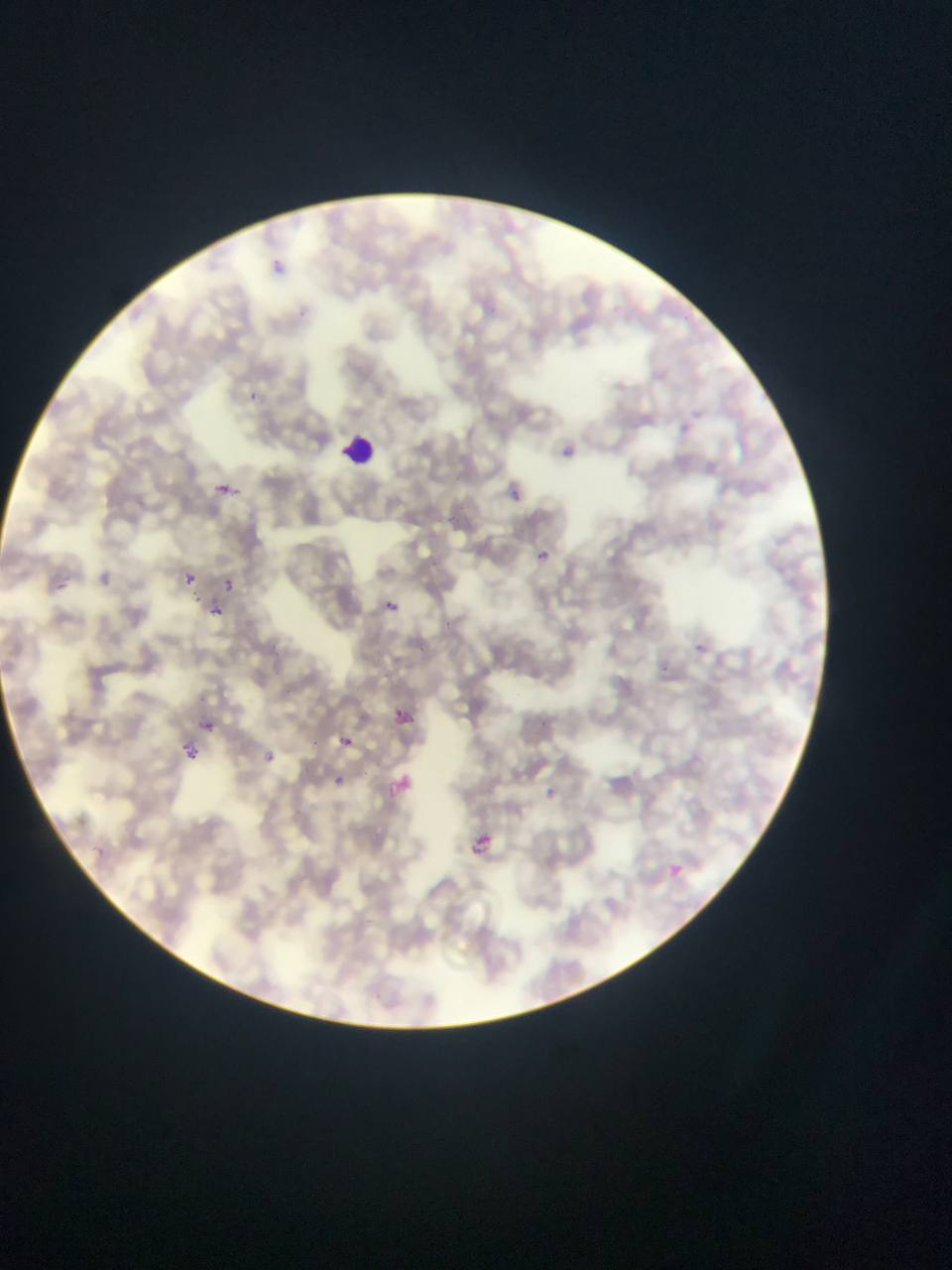 Approximate bounding boxes as (left, top, right, bottom) in pixels. Malaria parasite locations: (268, 257, 295, 281), (246, 388, 266, 402), (561, 441, 582, 463), (216, 479, 238, 503), (502, 482, 519, 501), (533, 547, 553, 566), (180, 571, 197, 587), (221, 576, 237, 592), (378, 596, 403, 619), (207, 603, 225, 620), (687, 639, 706, 658), (388, 703, 418, 732), (194, 713, 221, 738), (333, 731, 360, 756), (177, 741, 205, 767), (254, 743, 282, 770), (325, 770, 351, 794), (382, 771, 416, 805), (463, 829, 502, 863), (662, 859, 688, 883). Leukocyte locations: (336, 430, 382, 472). Photographed through a microscope with a mobile-phone camera. Thin blood film. Single field of view. Collected in Ghana. Image is 952×1270 pixels.